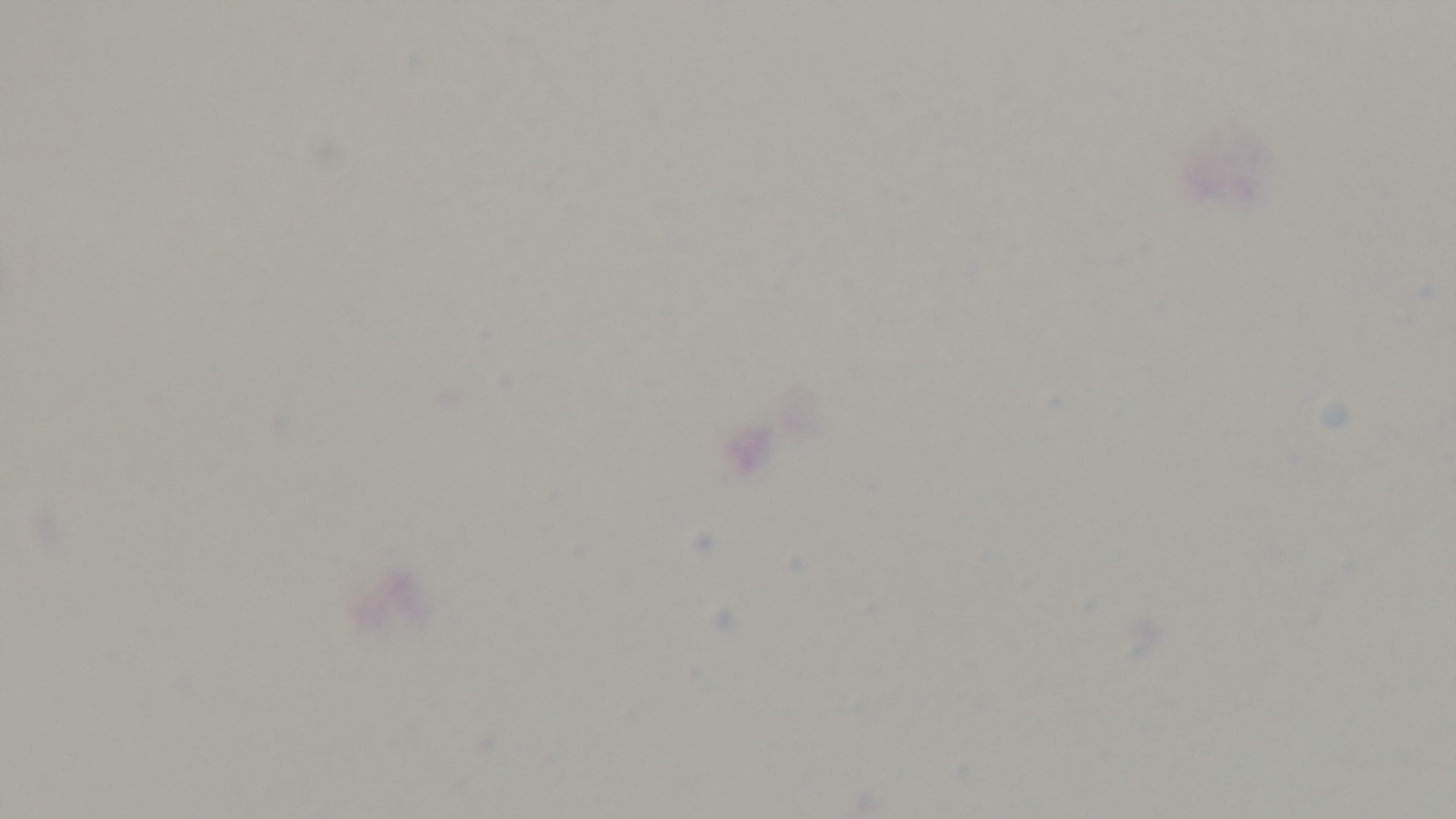
Captured with a mounted 4K digital camera. Single field of view. Light microscopy. Malaria status: negative. Preparation: thick. Giemsa-stained. Oil-immersion objective, 100x.